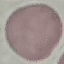

malaria status = uninfected
preparation = thin blood smear
capture = smartphone camera at the microscope eyepiece
stain = Giemsa
image type = automatically extracted cell patch, resized to 64 × 64 pixels